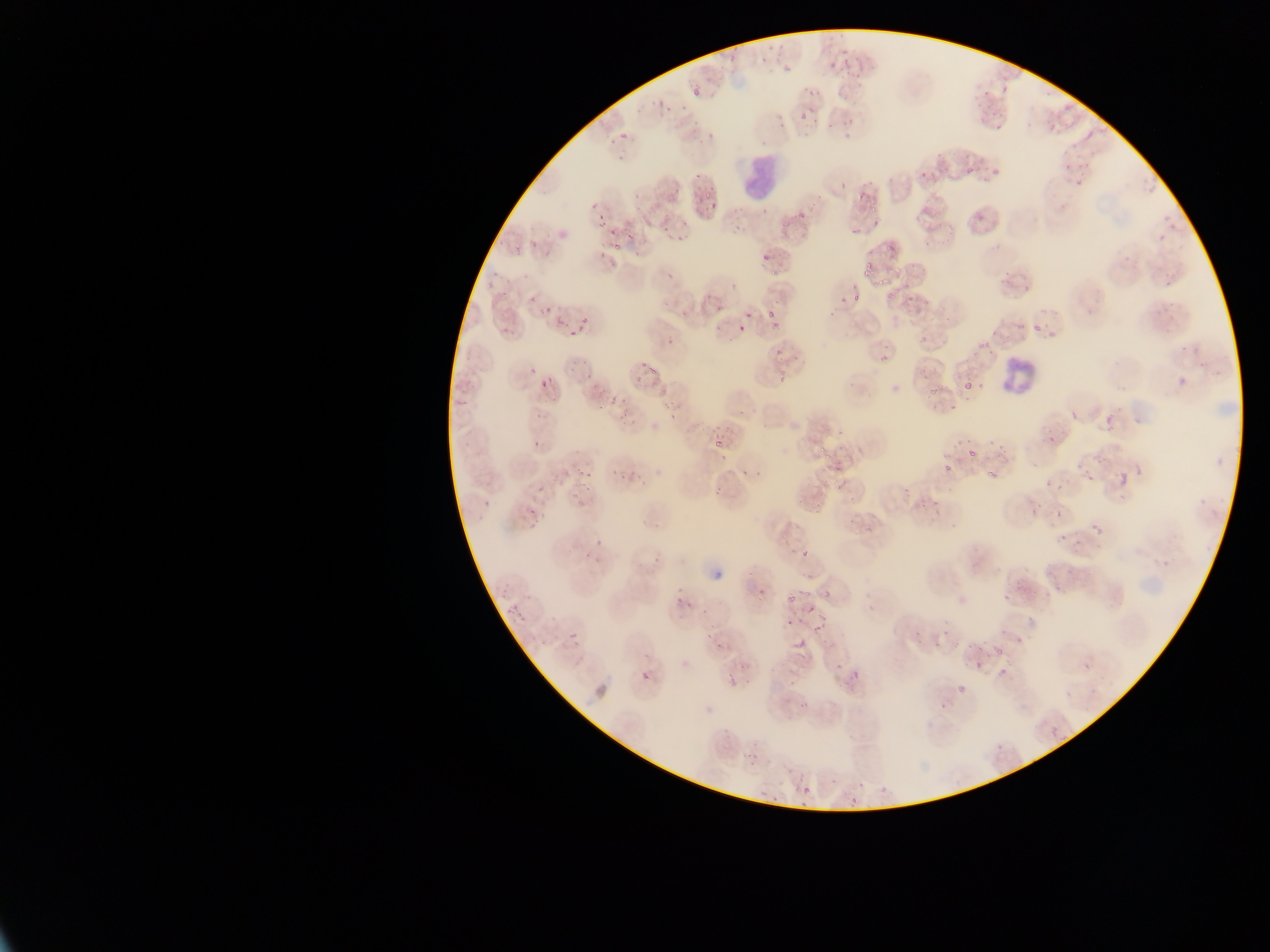
Approximate bounding boxes as [left, top, right, bottom] in pixels. Leukocyte locations: [735, 150, 783, 205], [1000, 358, 1035, 399]. Malaria parasite locations: [757, 46, 771, 62], [828, 50, 842, 72], [780, 54, 794, 76], [997, 82, 1011, 98], [692, 85, 703, 99], [660, 103, 671, 114], [795, 104, 809, 125], [823, 111, 840, 131], [976, 118, 983, 128], [1046, 118, 1064, 134], [617, 121, 630, 144], [691, 123, 703, 134], [613, 143, 631, 165], [1060, 155, 1074, 171], [993, 160, 1003, 182], [957, 165, 977, 175], [917, 172, 931, 182], [702, 187, 714, 198], [585, 199, 603, 211], [703, 206, 714, 214], [595, 211, 603, 227], [680, 214, 693, 236], [973, 215, 984, 221], [659, 221, 675, 234], [845, 225, 861, 240], [611, 227, 621, 239], [677, 234, 691, 248], [527, 236, 539, 244], [760, 240, 778, 260], [864, 260, 874, 272], [665, 267, 675, 289], [872, 268, 891, 289], [485, 273, 498, 295], [882, 280, 899, 302], [523, 290, 537, 304], [851, 290, 862, 305], [838, 294, 848, 304], [713, 298, 727, 311], [761, 301, 783, 317], [541, 303, 553, 316], [574, 316, 592, 329], [553, 319, 571, 327], [763, 319, 784, 332], [1029, 322, 1043, 333], [736, 323, 748, 335], [501, 325, 514, 339], [710, 325, 721, 336], [568, 332, 577, 338], [662, 343, 677, 351], [769, 346, 787, 360], [870, 354, 888, 365], [565, 356, 583, 369], [639, 357, 650, 378], [780, 367, 793, 385], [525, 370, 535, 376], [958, 372, 977, 393], [585, 373, 595, 380], [632, 375, 640, 385], [537, 377, 553, 387], [592, 385, 603, 398], [924, 389, 935, 399], [608, 392, 618, 405], [667, 400, 677, 419], [538, 405, 549, 419], [1100, 410, 1120, 433], [616, 418, 628, 430], [710, 418, 725, 434], [1042, 429, 1063, 451], [531, 434, 543, 447], [711, 439, 723, 452], [960, 443, 978, 459], [614, 457, 636, 487], [942, 462, 955, 476], [738, 466, 748, 476], [982, 466, 996, 481], [1115, 470, 1131, 488], [574, 471, 591, 483], [1083, 471, 1098, 486], [752, 472, 764, 482], [534, 483, 547, 494], [1047, 484, 1057, 494], [713, 485, 723, 497], [573, 491, 583, 505], [481, 498, 493, 512], [524, 502, 534, 520], [915, 503, 934, 514], [1052, 509, 1062, 519], [1022, 511, 1044, 530], [1088, 521, 1106, 540], [1059, 532, 1073, 546], [801, 546, 815, 558], [579, 547, 592, 560], [756, 582, 765, 600], [675, 590, 686, 608], [783, 590, 796, 603], [997, 590, 1011, 604], [806, 600, 814, 610], [679, 601, 701, 620], [500, 603, 521, 617], [785, 616, 797, 628], [814, 621, 827, 631], [568, 631, 581, 644], [706, 633, 713, 644], [793, 633, 811, 647], [715, 642, 729, 649], [994, 645, 1007, 655], [968, 660, 986, 674], [996, 665, 1009, 676], [843, 667, 863, 689], [641, 669, 653, 682], [726, 672, 736, 687], [955, 682, 968, 696], [796, 699, 813, 709], [1046, 722, 1064, 743], [994, 737, 1007, 751], [747, 747, 760, 760], [877, 782, 893, 792], [800, 784, 812, 796], [759, 788, 767, 798], [845, 791, 859, 805] | approximate [x, y] pixel centers of objects too small to bound: [615, 250], [658, 395], [596, 546]. Image is 1270×952 pixels. Thin blood smear. Single field of view. Sample from Ghana. Photographed through a microscope with a mobile-phone camera.